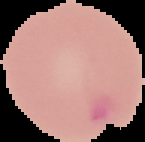
Summary:
  - Image type: cell region segmented out of the field of view; surrounding area masked to black
  - Malaria status: parasitized
  - Preparation: thin blood film
  - Image size: 145×142 pixels